Comment on the morphology of the red blood cells.
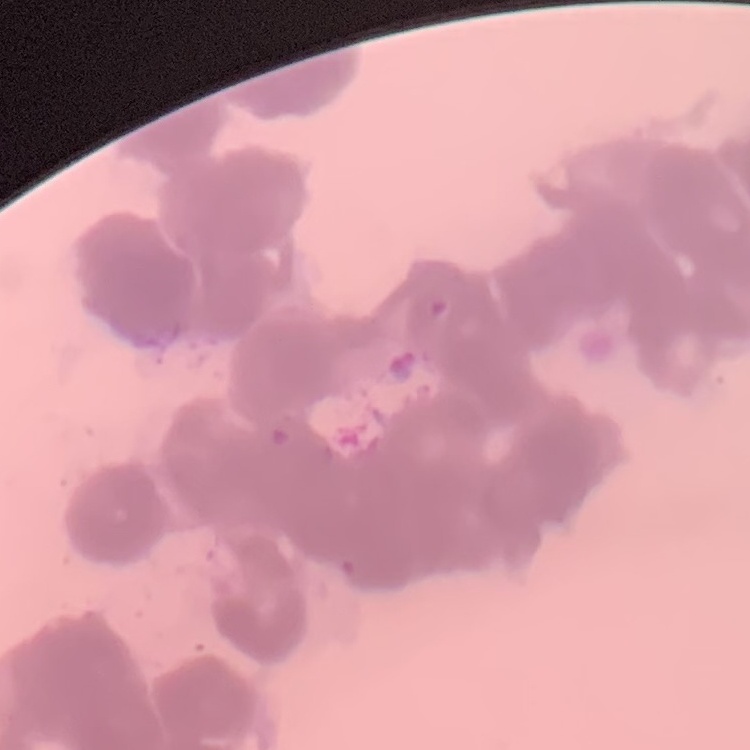

They show rouleaux formation.

Stained with either Field's or Giemsa. Thin peripheral smear. Square crop of a larger photomicrograph.